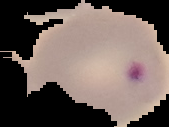
Malaria status: parasitized. Image is 169×127 pixels. The area outside the segmented cell region is set to black. From a thin blood smear.